Assess this cell for malaria.
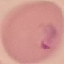

It is parasitized.

capture: smartphone through the microscope eyepiece
preparation: thin blood film
stain: Giemsa
image_type: automatically extracted cell patch, resized to 64 × 64 pixels